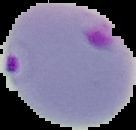 Malaria status: parasitized. Image is 136×130 pixels. From a thin blood film. The area outside the segmented cell region is set to black.